Identify the parasite.
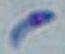

This is Toxoplasma gondii.

Summary:
  - Magnification: 1000x
  - Modality: photomicrograph